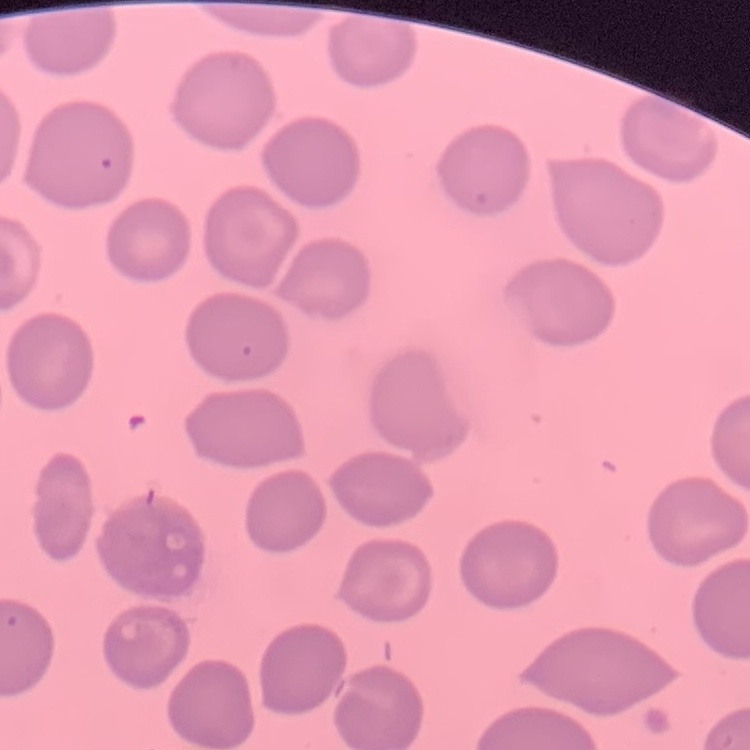

erythrocyte_morphology: no rouleaux formation
image_type: square crop of a larger photomicrograph
stain: Field's or Giemsa
preparation: thin blood film